State which cell type is depicted.
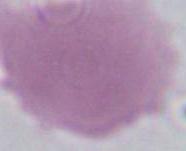
This is an erythrocyte.

Micrograph. Captured at 1000x magnification.